Report the malaria status of this cell.
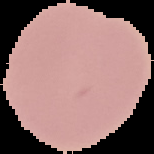

It is uninfected.

image size = 154×154 pixels
image type = segmented cell region with the area outside set to black
preparation = thin blood film